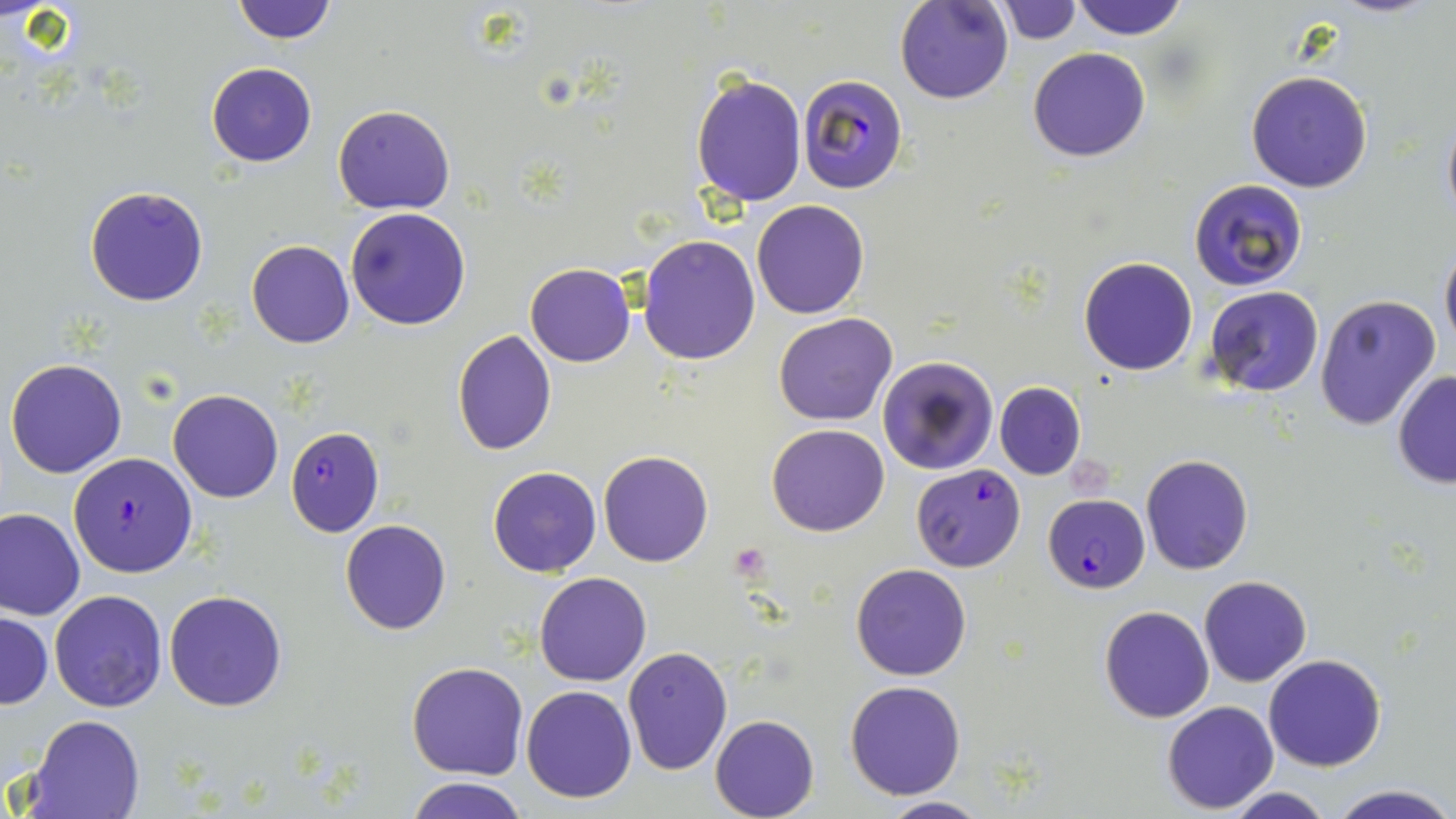
slide_level_diagnosis: Plasmodium falciparum
magnification: 1000x
modality: optical microscopy
preparation: thin blood film
uninfected_red_blood_cell_locations: 'approximate bounding boxes as (x1,y1)-(x2,y2) corner pairs in pixels: (230,0)-(340,45), (896,0)-(1014,105), (1069,0)-(1189,41), (996,1)-(1081,45), (1028,47)-(1150,162), (206,63)-(316,166), (1245,70)-(1373,193), (690,72)-(807,208), (334,102)-(455,214), (1440,110)-(1456,229), (1188,179)-(1307,290), (84,185)-(209,307), (751,199)-(869,319), (346,208)-(472,330), (639,235)-(762,365), (246,239)-(355,348), (1439,240)-(1456,361), (1078,257)-(1198,375), (524,263)-(634,366), (1206,287)-(1324,397), (1313,293)-(1442,432), (772,313)-(897,426), (453,330)-(557,456), (877,356)-(997,475), (6,357)-(127,478), (1391,370)-(1456,488), (995,381)-(1086,480), (168,389)-(283,504), (767,423)-(889,536), (599,450)-(713,568), (1141,454)-(1253,575), (488,466)-(602,578), (0,507)-(84,620), (340,519)-(452,635), (850,564)-(972,681), (535,572)-(652,687), (1199,575)-(1311,686), (49,589)-(167,712), (163,590)-(287,711), (1099,605)-(1214,722), (1,611)-(52,708), (622,646)-(734,776), (1263,653)-(1385,771), (407,661)-(529,779), (845,680)-(966,800), (521,684)-(637,803), (1162,700)-(1279,814), (25,715)-(145,819), (710,715)-(819,819), (404,776)-(532,819), (1219,785)-(1335,819), (1327,785)-(1456,819), (877,795)-(990,818)'
plasmodium_falciparum_infected_red_blood_cell_locations: 'approximate bounding boxes as (x1,y1)-(x2,y2) corner pairs in pixels: (796,72)-(910,194), (286,426)-(386,536), (70,452)-(196,575), (912,465)-(1024,572), (1042,493)-(1150,593)'
platelet_locations: 'approximate bounding boxes as (x1,y1)-(x2,y2) corner pairs in pixels: (731,541)-(772,579)'
stain: May-Grünwald-Giemsa
image_size: 1456×819 pixels
field_of_view: one of a larger specimen